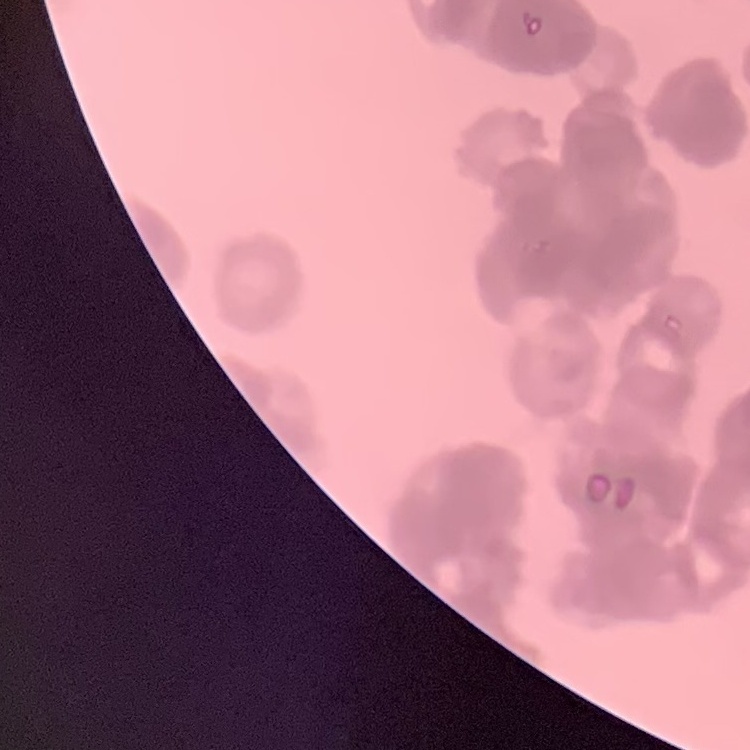
The erythrocytes show rouleaux formation. One tile cut from a larger photomicrograph. Thin blood film. Field's or Giemsa stain.